Assess this cell for malaria.
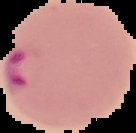

Parasitized.

{
  "image_size": "136×133 pixels",
  "preparation": "thin blood smear",
  "image_type": "segmented cell region on a black background"
}